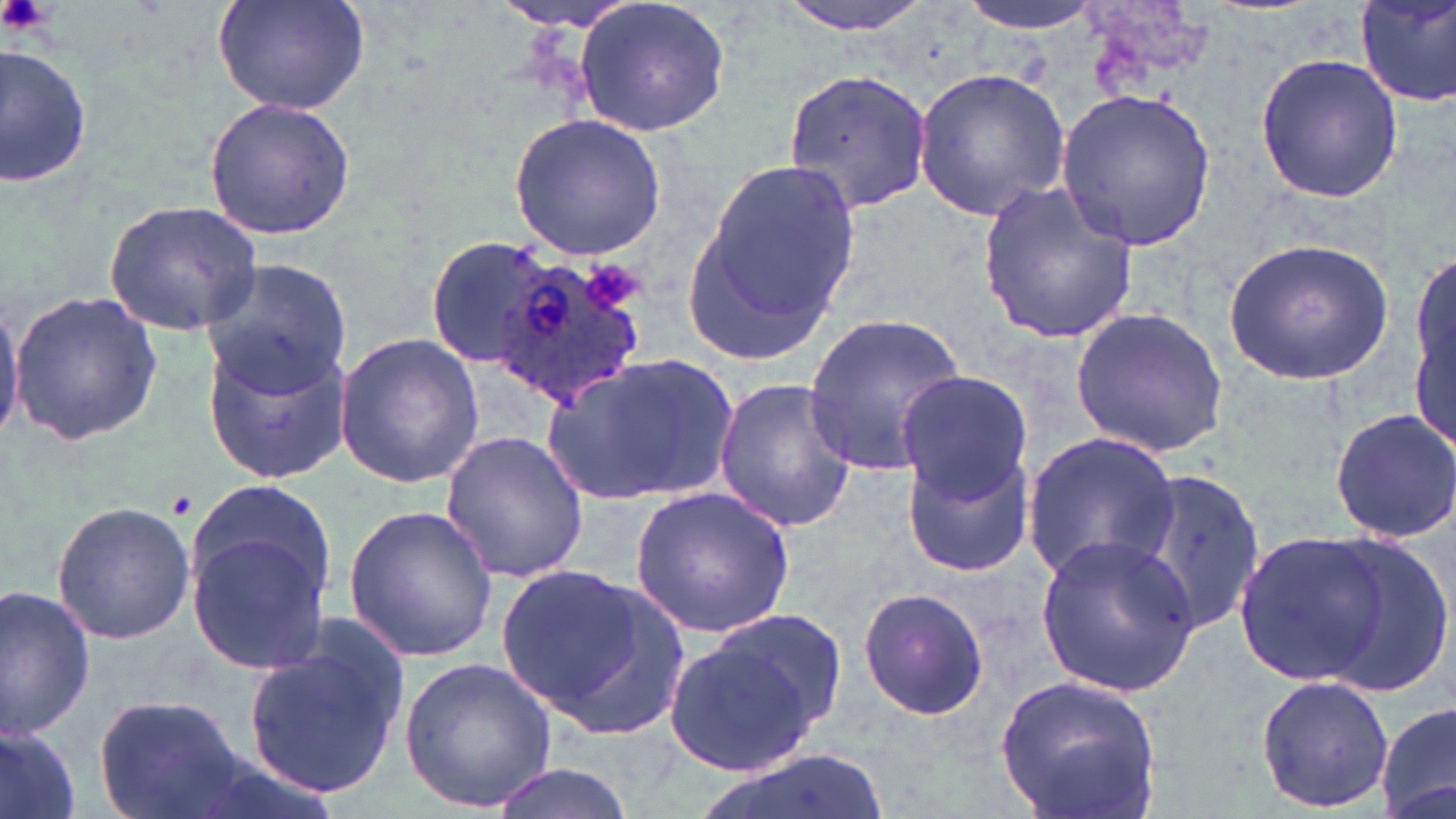

Summary:
  - Coordinate format: approximate bounding boxes as named x1/y1/x2/y2 corners in pixels
  - Platelet locations: (x1=2, y1=0, x2=54, y2=36), (x1=582, y1=259, x2=647, y2=315)
  - Uninfected red blood cell locations: (x1=212, y1=0, x2=373, y2=117), (x1=488, y1=0, x2=653, y2=32), (x1=573, y1=0, x2=732, y2=138), (x1=772, y1=0, x2=946, y2=36), (x1=957, y1=0, x2=1105, y2=36), (x1=1355, y1=0, x2=1456, y2=106), (x1=1077, y1=3, x2=1212, y2=107), (x1=0, y1=39, x2=92, y2=190), (x1=1253, y1=52, x2=1404, y2=204), (x1=913, y1=67, x2=1070, y2=221), (x1=782, y1=68, x2=935, y2=214), (x1=1057, y1=87, x2=1216, y2=251), (x1=202, y1=97, x2=356, y2=239), (x1=510, y1=114, x2=667, y2=257), (x1=688, y1=157, x2=863, y2=354), (x1=979, y1=179, x2=1141, y2=345), (x1=105, y1=198, x2=265, y2=334), (x1=423, y1=234, x2=566, y2=369), (x1=1224, y1=236, x2=1392, y2=386), (x1=199, y1=257, x2=355, y2=394), (x1=1411, y1=261, x2=1456, y2=441), (x1=9, y1=291, x2=163, y2=445), (x1=0, y1=292, x2=23, y2=443), (x1=1068, y1=306, x2=1230, y2=457), (x1=803, y1=314, x2=968, y2=478), (x1=203, y1=327, x2=351, y2=485), (x1=335, y1=330, x2=484, y2=488), (x1=548, y1=353, x2=740, y2=504), (x1=895, y1=370, x2=1032, y2=499), (x1=713, y1=378, x2=859, y2=535), (x1=1327, y1=405, x2=1456, y2=545), (x1=439, y1=430, x2=591, y2=585), (x1=1022, y1=432, x2=1179, y2=585), (x1=901, y1=443, x2=1035, y2=578), (x1=1135, y1=464, x2=1267, y2=643), (x1=180, y1=484, x2=339, y2=677), (x1=629, y1=487, x2=795, y2=638), (x1=48, y1=499, x2=196, y2=645), (x1=342, y1=504, x2=499, y2=664), (x1=1231, y1=528, x2=1395, y2=687), (x1=1033, y1=534, x2=1204, y2=697), (x1=1317, y1=537, x2=1454, y2=699), (x1=493, y1=563, x2=681, y2=734), (x1=0, y1=585, x2=96, y2=740), (x1=856, y1=586, x2=991, y2=721), (x1=704, y1=605, x2=849, y2=742), (x1=241, y1=616, x2=410, y2=803), (x1=661, y1=633, x2=827, y2=780), (x1=401, y1=655, x2=558, y2=811), (x1=997, y1=674, x2=1161, y2=819), (x1=1254, y1=675, x2=1394, y2=814), (x1=95, y1=695, x2=250, y2=819), (x1=1376, y1=702, x2=1455, y2=819), (x1=1, y1=723, x2=83, y2=819), (x1=703, y1=749, x2=892, y2=819), (x1=484, y1=764, x2=641, y2=819)
  - Plasmodium ovale-infected red blood cell locations: (x1=483, y1=245, x2=647, y2=408)
  - Slide-level diagnosis: Plasmodium ovale
  - Image size: 1456×819 pixels
  - Stain: May-Grünwald-Giemsa
  - Modality: optical microscopy
  - Magnification: 1000x
  - Field of view: single
  - Preparation: thin blood film